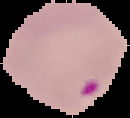
Segmented cell region on a black background. Image is 130×118 pixels. From a thin blood smear. Result: Plasmodium parasites detected.